State the blood parasite species.
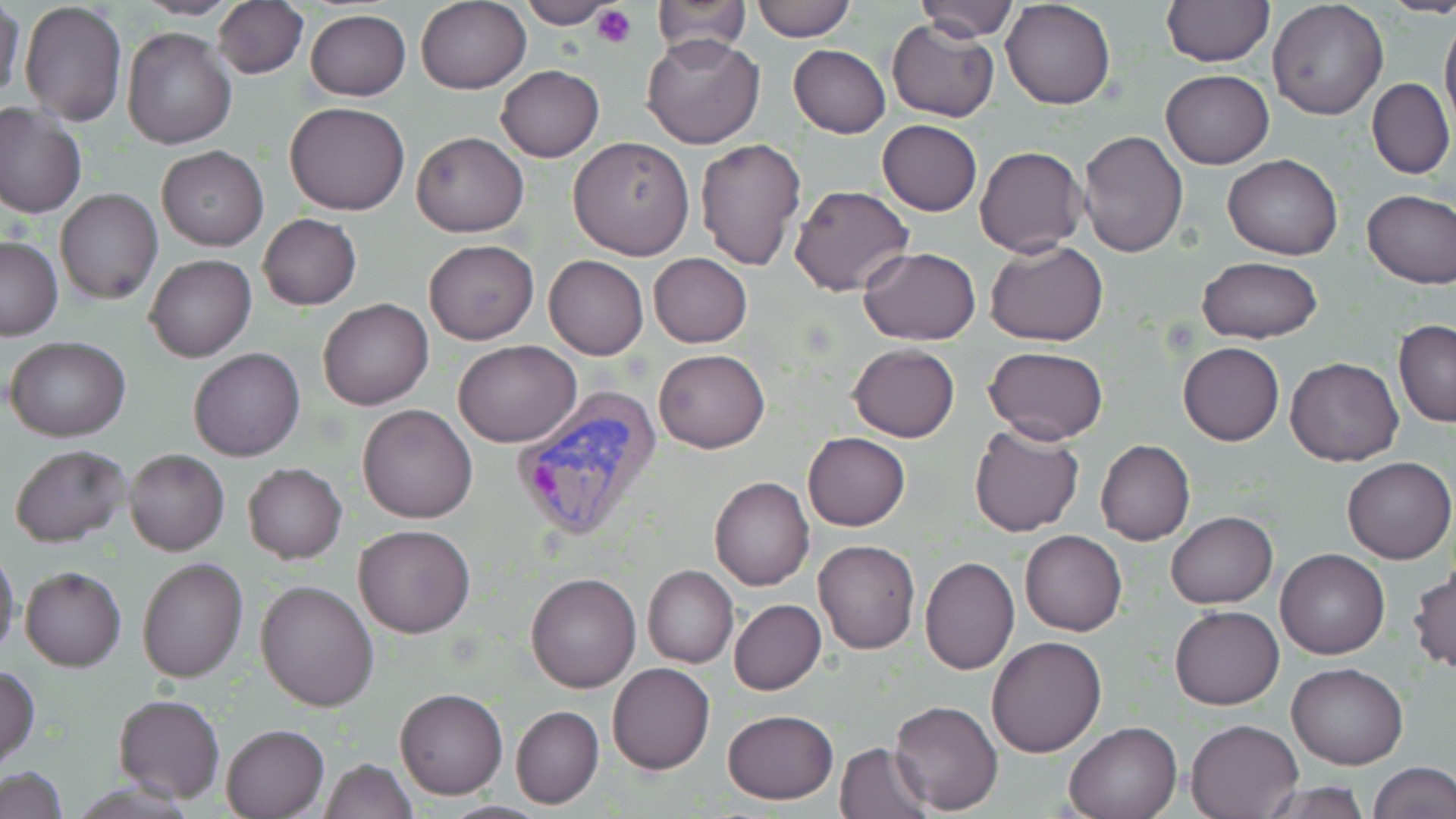

Plasmodium vivax.

Summary:
  - Coordinate format: approximate bounding boxes as [x1, y1, x2, y2] in pixels
  - Plasmodium vivax-infected red blood cell locations: [510, 387, 663, 543]
  - Platelet locations: [592, 4, 636, 49]
  - Uninfected red blood cell locations: [1, 0, 25, 110], [133, 0, 242, 20], [211, 0, 309, 78], [518, 0, 621, 28], [913, 0, 1018, 41], [1003, 0, 1116, 109], [1160, 0, 1275, 67], [750, 1, 856, 42], [1268, 1, 1388, 121], [19, 2, 128, 126], [416, 2, 530, 93], [649, 2, 750, 59], [304, 9, 411, 101], [1440, 10, 1456, 134], [886, 19, 999, 122], [121, 25, 236, 149], [640, 33, 764, 150], [788, 44, 891, 138], [496, 65, 604, 162], [1161, 69, 1273, 168], [1367, 77, 1454, 180], [285, 101, 409, 216], [0, 103, 85, 218], [877, 119, 982, 216], [412, 131, 527, 237], [1077, 131, 1188, 258], [567, 137, 694, 260], [695, 139, 808, 271], [156, 144, 269, 251], [974, 145, 1086, 258], [1222, 153, 1343, 260], [789, 185, 913, 296], [55, 189, 162, 305], [1361, 189, 1456, 287], [257, 213, 362, 311], [0, 237, 63, 339], [424, 239, 538, 345], [985, 240, 1109, 346], [859, 247, 982, 343], [647, 253, 752, 348], [144, 254, 256, 362], [544, 256, 649, 360], [1196, 256, 1323, 343], [317, 297, 434, 410], [1393, 319, 1456, 428], [6, 336, 131, 441], [453, 341, 582, 447], [1178, 342, 1285, 445], [849, 343, 960, 441], [189, 347, 305, 462], [984, 347, 1109, 445], [653, 350, 771, 454], [1285, 356, 1405, 467], [357, 403, 478, 524], [968, 425, 1084, 536], [803, 432, 910, 531], [1095, 440, 1195, 546], [9, 443, 132, 547], [125, 449, 228, 555], [1342, 457, 1455, 564], [243, 463, 347, 564], [710, 477, 813, 591], [1166, 511, 1277, 608], [355, 524, 474, 639], [1020, 530, 1127, 636], [813, 540, 921, 654], [0, 546, 20, 660], [1275, 548, 1390, 660], [919, 556, 1019, 675], [137, 557, 247, 683], [642, 565, 737, 668], [21, 567, 127, 672], [1409, 568, 1455, 673], [526, 570, 640, 692], [255, 579, 380, 711], [729, 599, 827, 695], [1170, 605, 1283, 710], [986, 635, 1107, 758], [1286, 662, 1409, 768], [607, 663, 714, 775], [0, 665, 39, 768], [395, 687, 508, 799], [112, 694, 226, 804], [890, 700, 1003, 815], [510, 705, 604, 809], [723, 709, 838, 805], [1185, 717, 1305, 819], [1063, 719, 1183, 818], [222, 724, 329, 817], [833, 742, 935, 818], [318, 758, 416, 818], [1369, 761, 1455, 818], [1, 767, 67, 818], [1254, 782, 1375, 817]
  - Preparation: thin blood smear
  - Magnification: 1000x
  - Stain: May-Grünwald-Giemsa
  - Modality: optical microscopy
  - Image size: 1456×819 pixels
  - Field of view: single